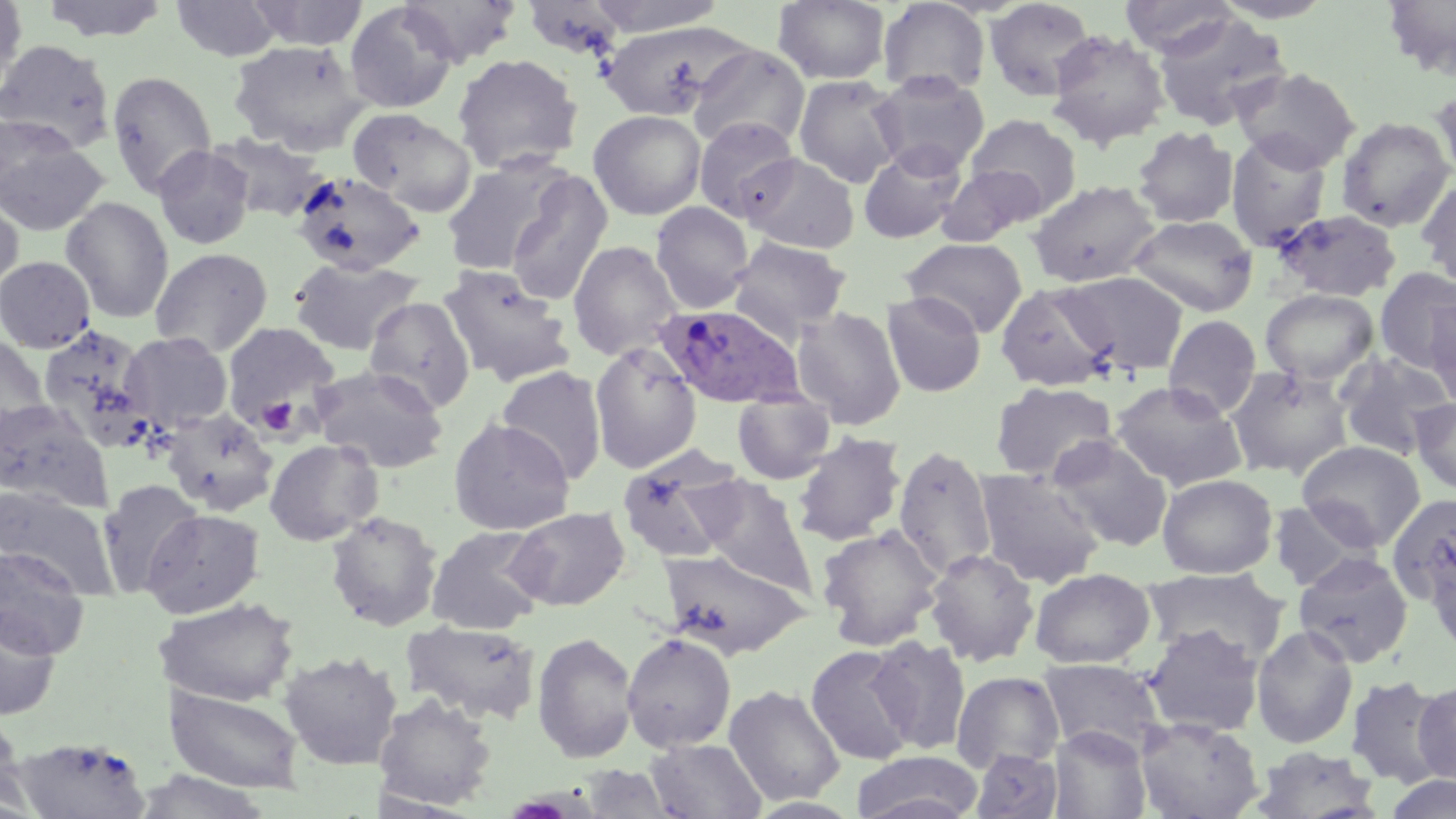 Approximate bounding boxes as [x1, y1, x2, y2] in pixels. Platelet locations: [256, 396, 300, 437]. Uninfected red blood cell locations: [0, 0, 27, 97], [39, 0, 171, 43], [246, 0, 369, 50], [398, 0, 521, 66], [584, 0, 729, 36], [773, 0, 891, 84], [983, 0, 1097, 100], [1119, 0, 1240, 58], [1209, 0, 1339, 23], [1382, 0, 1456, 81], [170, 1, 283, 61], [877, 1, 991, 97], [344, 2, 460, 114], [522, 2, 627, 60], [1152, 11, 1291, 132], [598, 20, 750, 122], [1045, 29, 1170, 149], [0, 39, 116, 153], [228, 40, 369, 154], [687, 44, 809, 152], [452, 53, 583, 175], [1231, 67, 1360, 172], [106, 69, 218, 198], [871, 72, 990, 177], [793, 74, 905, 188], [1431, 86, 1456, 184], [347, 108, 477, 216], [588, 110, 706, 220], [966, 114, 1082, 216], [693, 115, 801, 223], [1336, 116, 1454, 232], [0, 120, 110, 237], [1133, 126, 1239, 228], [210, 132, 334, 223], [1225, 132, 1333, 249], [152, 145, 256, 250], [857, 145, 968, 244], [741, 153, 860, 254], [439, 155, 572, 276], [937, 165, 1045, 247], [291, 171, 426, 277], [505, 172, 613, 307], [1416, 178, 1456, 291], [1028, 179, 1162, 288], [0, 192, 24, 302], [60, 196, 175, 323], [651, 201, 754, 314], [1271, 209, 1402, 301], [1127, 214, 1259, 317], [728, 236, 853, 338], [902, 237, 1028, 337], [567, 240, 683, 360], [149, 247, 273, 357], [0, 255, 97, 354], [287, 257, 424, 356], [437, 263, 575, 386], [1375, 267, 1456, 373], [1061, 270, 1189, 375], [995, 281, 1119, 393], [1260, 289, 1379, 386], [881, 291, 986, 397], [1425, 296, 1456, 409], [363, 297, 475, 412], [791, 306, 907, 429], [1163, 314, 1261, 418], [220, 321, 341, 430], [36, 323, 156, 449], [119, 331, 234, 433], [0, 333, 54, 442], [589, 341, 703, 473], [1333, 352, 1455, 460], [310, 365, 447, 473], [495, 365, 608, 483], [1225, 365, 1355, 480], [1110, 380, 1248, 490], [990, 381, 1117, 482], [731, 391, 837, 484], [1410, 398, 1456, 495], [0, 400, 110, 510], [161, 409, 279, 516], [448, 417, 576, 535], [790, 431, 907, 546], [1046, 435, 1173, 551], [264, 438, 383, 545], [1296, 440, 1426, 550], [893, 444, 998, 580], [616, 448, 749, 564], [974, 468, 1107, 589], [1157, 473, 1278, 579], [693, 476, 816, 594], [97, 479, 204, 597], [0, 486, 117, 597], [1387, 493, 1456, 606], [1267, 499, 1378, 592], [504, 506, 631, 611], [140, 508, 264, 618], [325, 511, 443, 631], [816, 524, 946, 649], [425, 525, 548, 635], [0, 547, 90, 659], [924, 548, 1040, 667], [655, 549, 812, 658], [1293, 552, 1415, 668], [1030, 567, 1156, 669], [1140, 567, 1290, 665], [161, 597, 299, 706], [0, 608, 61, 721], [401, 621, 541, 724], [1142, 624, 1265, 737], [1250, 624, 1359, 748], [531, 631, 639, 762], [621, 633, 737, 751], [867, 636, 971, 754], [805, 644, 917, 765], [278, 650, 403, 771], [1037, 658, 1167, 758], [951, 670, 1064, 773], [1345, 675, 1450, 788], [1412, 679, 1456, 784], [724, 684, 846, 806], [165, 685, 304, 794], [373, 693, 498, 811], [0, 710, 24, 813], [1135, 717, 1263, 819], [1048, 726, 1152, 819], [10, 736, 151, 818], [645, 738, 767, 819], [1248, 746, 1382, 818], [969, 749, 1065, 819], [850, 750, 984, 819], [578, 764, 681, 819], [130, 770, 274, 819], [1383, 776, 1456, 819]. Plasmodium ovale-infected red blood cell locations: [654, 303, 805, 409]. Slide-level diagnosis: Plasmodium ovale. Captured at 1000x magnification. Thin blood film. Optical microscopy. Image is 1456×819 pixels. May-Grünwald-Giemsa stain. Single field of view.